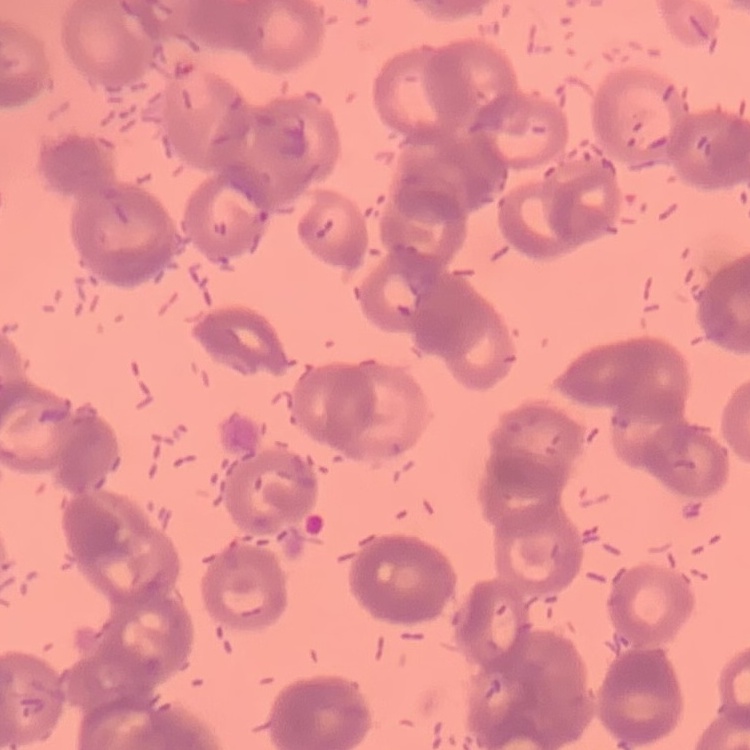
Summary:
  - Red blood cell morphology: rouleaux formation
  - Preparation: thin blood film
  - Image type: square crop of a larger photomicrograph
  - Stain: Field's or Giemsa